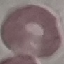 Malaria status: uninfected. Automatically extracted cell patch, resized to 64 × 64 pixels. Giemsa-stained preparation. Acquired by smartphone through the microscope eyepiece. Thin smear of blood.